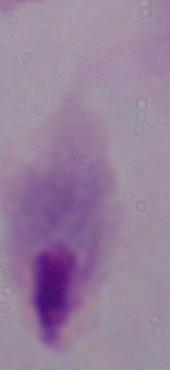
Summary:
  - Modality: photomicrograph
  - Identification: trichomonad
  - Magnification: 1000x